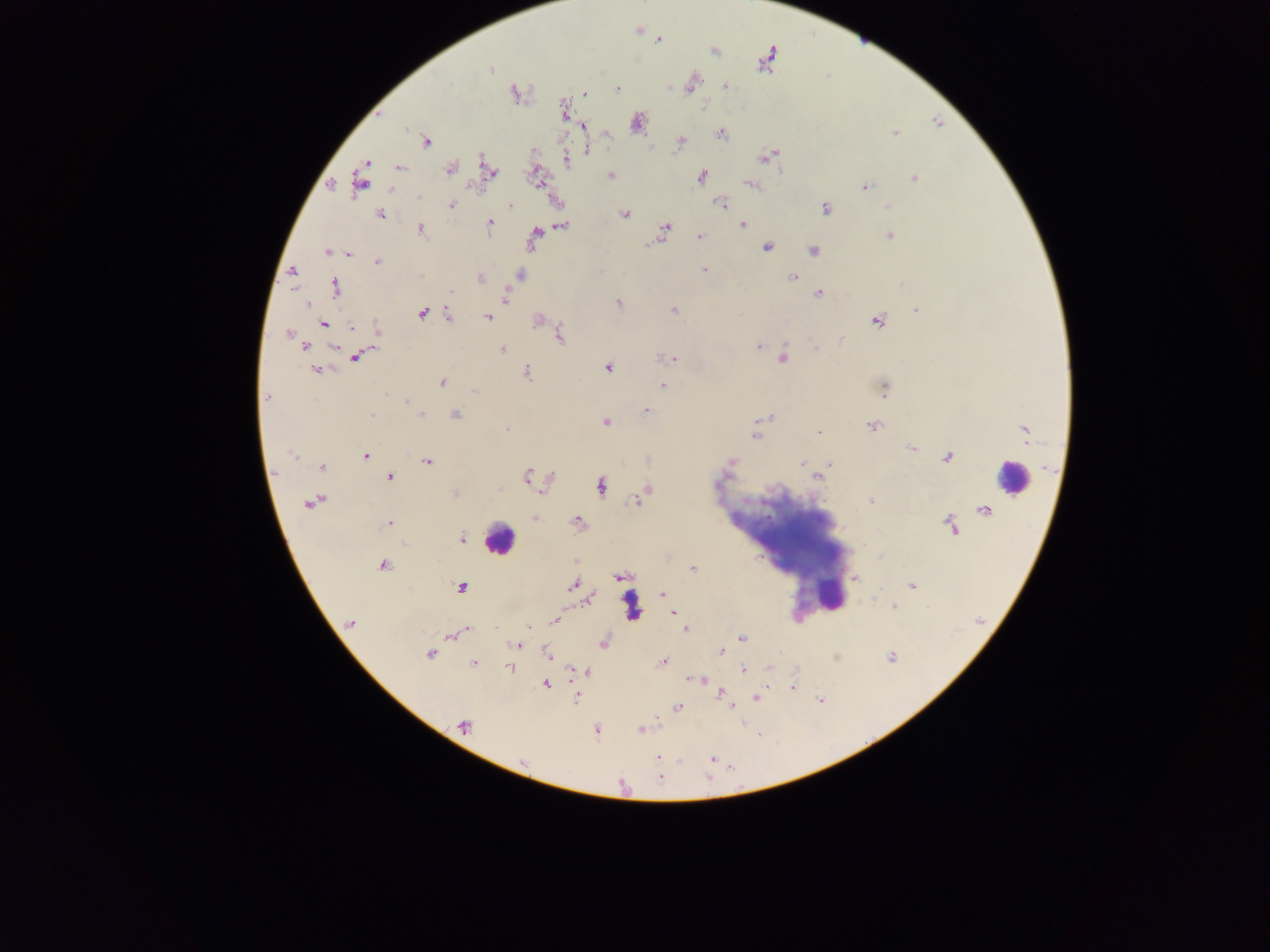
malaria parasite locations = approximate centers as {x, y} in pixels: {638, 29}, {657, 40}, {714, 50}, {767, 60}, {490, 68}, {691, 82}, {725, 86}, {616, 88}, {514, 92}, {584, 93}, {564, 110}, {636, 123}, {584, 125}, {605, 132}, {894, 132}, {720, 133}, {426, 141}, {680, 141}, {585, 149}, {768, 156}, {566, 159}, {365, 162}, {400, 167}, {449, 169}, {488, 170}, {536, 175}, {611, 175}, {700, 175}, {914, 178}, {361, 182}, {331, 184}, {751, 185}, {864, 187}, {721, 203}, {510, 204}, {450, 205}, {888, 207}, {825, 208}, {624, 214}, {380, 215}, {488, 223}, {741, 224}, {561, 225}, {420, 228}, {663, 231}, {890, 234}, {699, 235}, {534, 236}, {767, 248}, {813, 249}, {327, 252}, {348, 255}, {377, 261}, {704, 270}, {292, 271}, {520, 274}, {793, 277}, {479, 278}, {335, 287}, {819, 292}, {505, 296}, {305, 303}, {618, 303}, {673, 310}, {917, 310}, {422, 312}, {447, 316}, {488, 316}, {537, 320}, {877, 320}, {322, 324}, {351, 327}, {377, 328}, {288, 333}, {559, 334}, {305, 346}, {334, 346}, {757, 346}, {502, 349}, {357, 355}, {782, 357}, {671, 358}, {608, 366}, {316, 369}, {526, 372}, {441, 382}, {662, 386}, {883, 388}, {475, 391}, {266, 397}, {407, 401}, {645, 409}, {455, 414}, {371, 415}, {422, 415}, {771, 417}, {605, 422}, {871, 425}, {505, 429}, {756, 431}, {1024, 431}, {820, 432}, {912, 447}, {365, 456}, {947, 457}, {428, 461}, {730, 462}, {803, 462}, {829, 464}, {321, 466}, {389, 476}, {527, 476}, {818, 476}, {550, 479}, {600, 486}, {646, 490}, {455, 494}, {312, 501}, {639, 501}, {870, 501}, {983, 510}, {533, 518}, {389, 522}, {577, 522}, {951, 526}, {461, 539}, {576, 561}, {382, 565}, {692, 569}, {618, 577}, {855, 578}, {911, 584}, {572, 585}, {461, 587}, {662, 594}, {587, 600}, {894, 608}, {672, 613}, {554, 621}, {350, 623}, {529, 628}, {685, 629}, {465, 630}, {459, 632}, {450, 635}, {741, 638}, {603, 643}, {517, 645}, {721, 650}, {546, 652}, {429, 653}, {891, 657}, {662, 662}, {473, 663}, {510, 668}, {743, 669}, {573, 670}, {587, 671}, {688, 678}, {700, 679}, {545, 684}, {792, 686}, {719, 693}, {576, 696}, {756, 698}, {821, 699}, {732, 705}, {677, 708}, {463, 725}, {640, 729}, {597, 730}, {657, 757}, {711, 758}, {523, 762}
capture = mobile-phone photograph through a microscope
field of view = single
country = Ghana
leukocyte locations = approximate centers as {x, y} in pixels: {1013, 478}, {498, 538}, {786, 547}, {833, 596}, {634, 607}
preparation = thick blood smear
image size = 1270×952 pixels